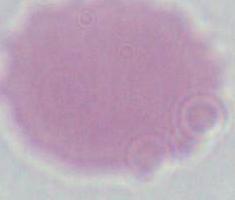
A red blood cell is seen. Captured at 1000x magnification. Micrograph.